State which parasite is depicted.
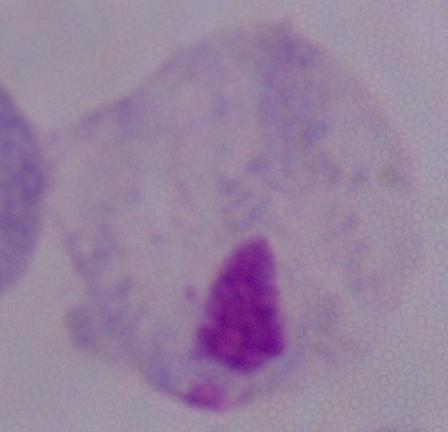
A trichomonad.

1000x magnification. Photomicrograph.